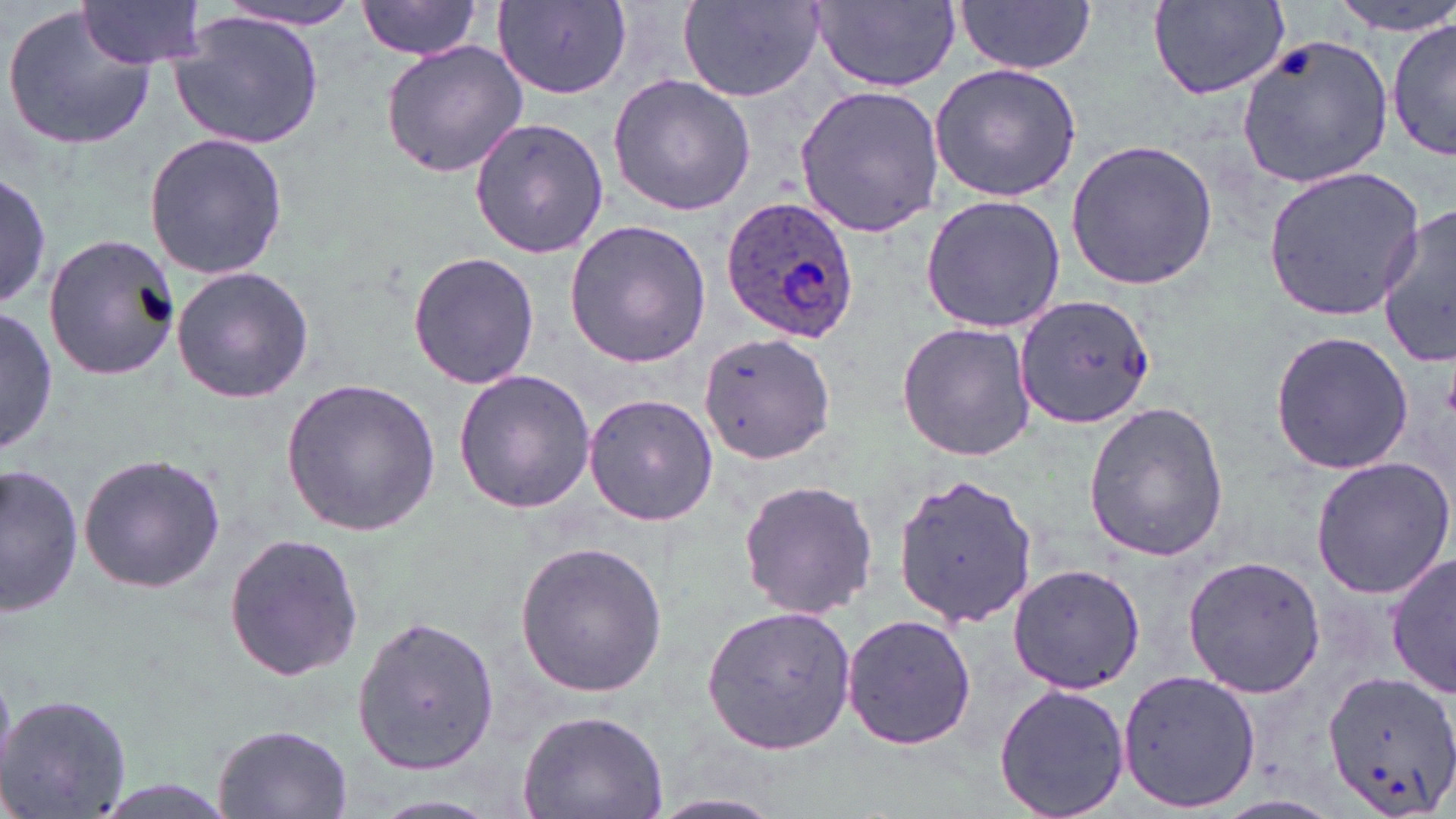

Approximate bounding boxes as (x1, y1, x2, y2) in pixels. Plasmodium ovale-infected red blood cell locations: (721, 196, 859, 345). Uninfected red blood cell locations: (76, 0, 210, 69), (356, 0, 487, 59), (677, 0, 826, 103), (1334, 0, 1452, 34), (1147, 1, 1291, 99), (210, 2, 363, 30), (494, 2, 629, 98), (813, 2, 961, 89), (957, 2, 1096, 77), (4, 5, 157, 151), (169, 12, 324, 152), (1387, 12, 1454, 165), (1236, 31, 1396, 190), (378, 40, 529, 179), (928, 62, 1083, 202), (607, 73, 759, 215), (795, 84, 946, 237), (466, 115, 609, 261), (143, 131, 289, 280), (1065, 139, 1217, 291), (1260, 165, 1428, 322), (0, 170, 52, 313), (919, 194, 1066, 334), (1370, 209, 1456, 365), (562, 219, 712, 369), (43, 233, 182, 381), (408, 250, 540, 391), (171, 266, 316, 403), (1013, 292, 1157, 431), (0, 309, 56, 457), (896, 320, 1036, 463), (1267, 328, 1416, 478), (697, 331, 835, 468), (452, 368, 597, 514), (280, 377, 441, 537), (583, 391, 717, 526), (1082, 400, 1229, 564), (78, 451, 226, 594), (1309, 455, 1454, 600), (1, 461, 86, 617), (894, 474, 1042, 629), (734, 477, 882, 622), (222, 530, 364, 683), (514, 540, 668, 698), (1387, 552, 1455, 698), (1181, 555, 1325, 699), (1008, 564, 1144, 693), (700, 603, 857, 755), (841, 611, 978, 753), (351, 612, 500, 773), (1320, 668, 1456, 817), (1118, 669, 1260, 812), (992, 681, 1131, 819), (0, 692, 130, 814), (518, 707, 669, 819), (212, 722, 353, 819), (649, 791, 788, 817). Slide-level diagnosis: Plasmodium ovale. One field of a larger specimen. Image is 1456×819 pixels. Thin blood film. May-Grünwald-Giemsa-stained preparation. Light microscopy. 1000x magnification.